State which parasite is depicted.
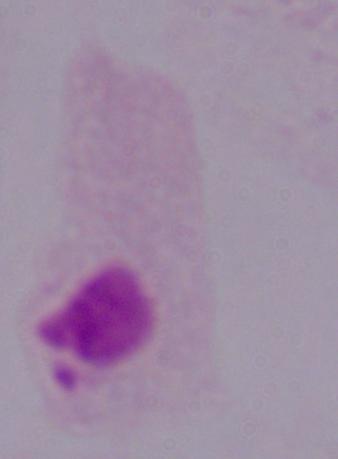
This is a trichomonad.

Summary:
  - Magnification: 1000x
  - Modality: micrograph